State which parasite is depicted.
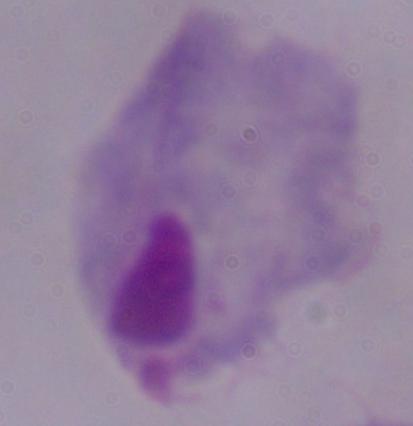
This is a trichomonad.

Micrograph. Captured at 1000x magnification.